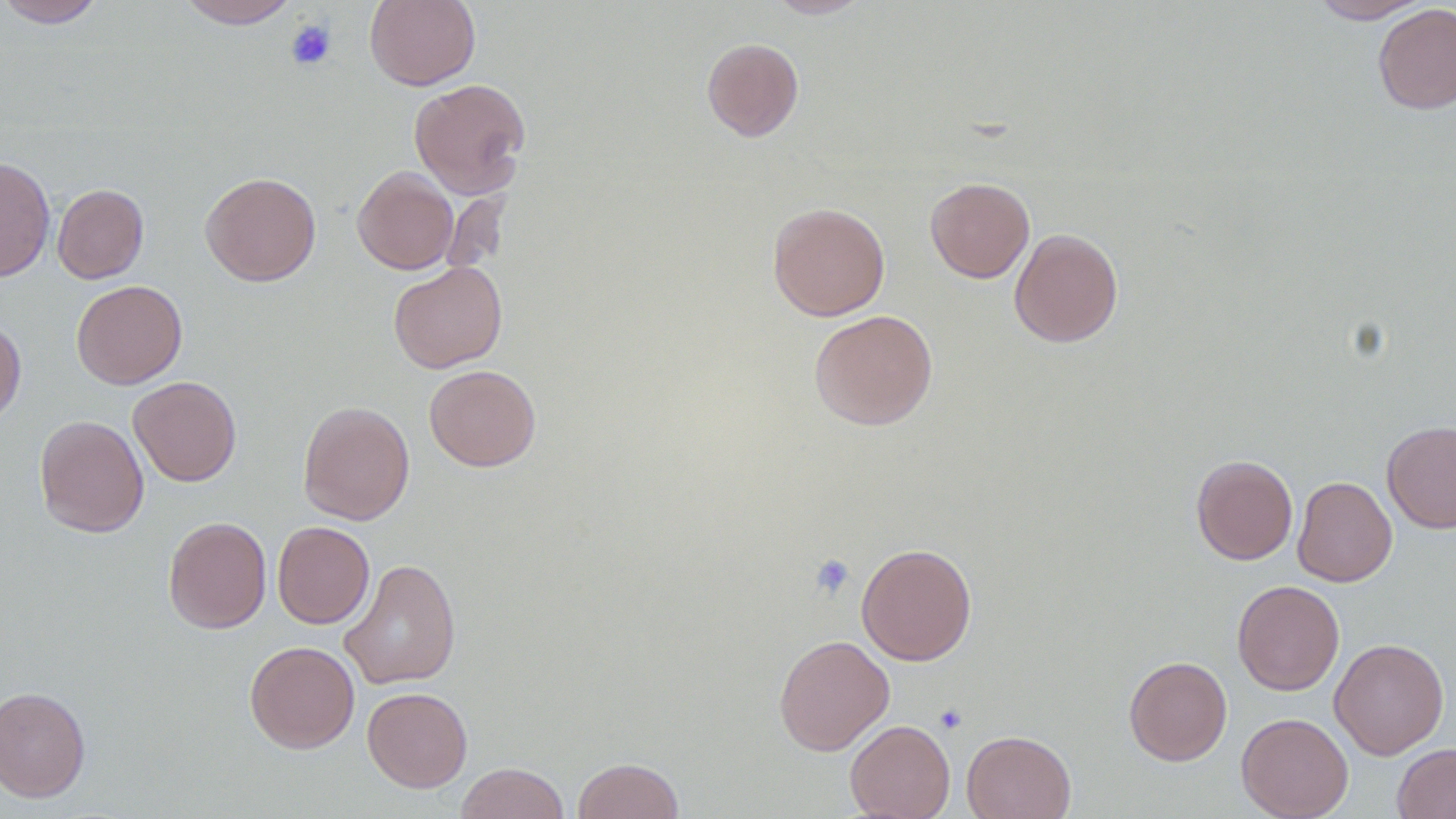

Summary:
  - Coordinate format: approximate bounding boxes as (x1, y1, x2, y2) in pixels
  - Platelet locations: (285, 19, 337, 70), (809, 553, 856, 598), (934, 703, 968, 734)
  - Uninfected red blood cell locations: (0, 0, 109, 28), (174, 0, 300, 28), (365, 0, 481, 90), (766, 0, 872, 18), (1310, 0, 1431, 23), (1373, 3, 1456, 114), (701, 37, 804, 142), (408, 77, 531, 198), (0, 156, 56, 282), (352, 166, 458, 274), (200, 171, 321, 286), (925, 177, 1035, 283), (52, 183, 149, 284), (767, 202, 890, 321), (1009, 228, 1123, 348), (388, 261, 508, 373), (71, 280, 187, 389), (809, 309, 938, 431), (0, 317, 26, 427), (424, 364, 541, 472), (128, 376, 242, 487), (298, 400, 415, 526), (34, 414, 149, 537), (1381, 420, 1456, 534), (1191, 454, 1298, 565), (1292, 476, 1397, 587), (163, 516, 271, 634), (272, 521, 375, 629), (856, 542, 977, 666), (339, 558, 461, 689), (1232, 579, 1344, 696), (773, 633, 894, 755), (1330, 638, 1449, 759), (245, 640, 359, 753), (1124, 656, 1232, 766), (0, 686, 91, 803), (362, 686, 473, 792), (1236, 712, 1354, 819), (845, 719, 955, 818), (962, 729, 1076, 818), (1392, 743, 1456, 819), (572, 757, 685, 819), (455, 762, 571, 819)
  - Slide-level diagnosis: no evidence of blood parasites
  - Field of view: one of a larger specimen
  - Modality: light microscopy
  - Preparation: thin blood film
  - Magnification: 1000x
  - Image size: 1456×819 pixels